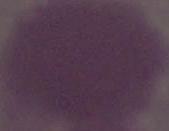 1000x magnification. An erythrocyte is seen. Micrograph.